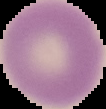

Image is 106×109 pixels. Malaria status: uninfected. Segmented cell region on a black background. From a thin blood film.